Identify the parasite.
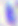
Toxoplasma gondii.

Summary:
  - Magnification: 400x
  - Modality: photomicrograph